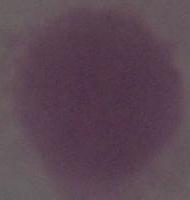
Summary:
  - Modality: photomicrograph
  - Identification: erythrocyte
  - Magnification: 1000x